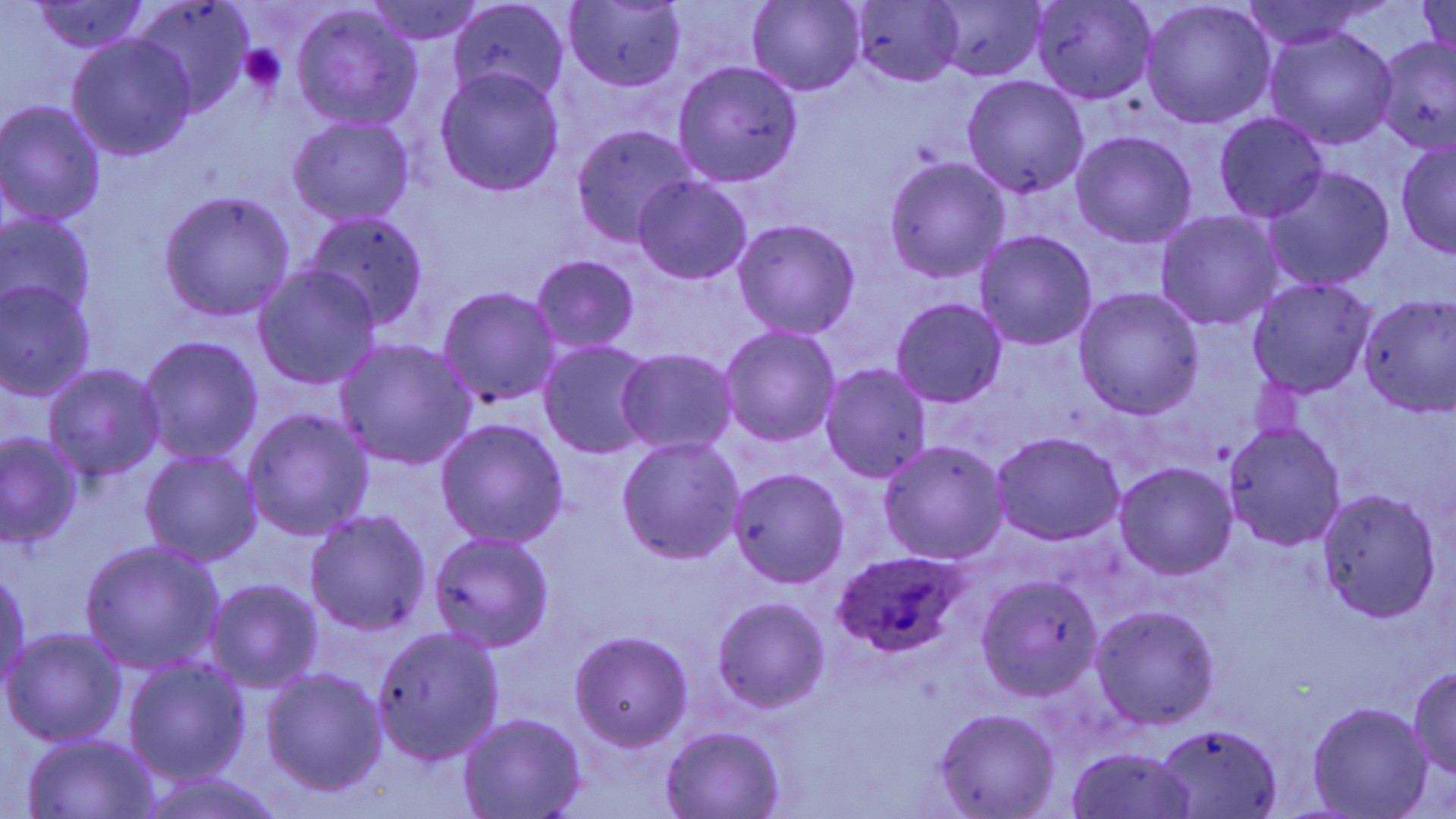
Approximate bounding boxes as (x1,y1)-(x2,y2) corner pairs in pixels. Uninfected red blood cell locations: (131,0)-(254,115), (365,0)-(489,45), (564,0)-(686,91), (746,0)-(865,96), (1031,0)-(1155,104), (1419,0)-(1454,62), (23,1)-(152,54), (449,2)-(571,106), (851,2)-(964,87), (927,2)-(1045,82), (1141,3)-(1276,127), (291,7)-(423,131), (1264,25)-(1400,148), (67,35)-(197,161), (1375,37)-(1455,155), (672,62)-(802,188), (435,68)-(565,196), (962,75)-(1090,198), (0,103)-(105,226), (1214,112)-(1330,222), (289,116)-(415,225), (571,125)-(696,245), (1070,130)-(1197,249), (1396,138)-(1455,257), (885,158)-(1010,283), (1263,164)-(1395,291), (635,177)-(752,284), (158,191)-(294,322), (307,210)-(429,326), (1155,211)-(1284,330), (1,213)-(98,321), (734,217)-(860,339), (977,230)-(1096,351), (532,255)-(639,354), (253,266)-(382,391), (1247,277)-(1379,396), (0,281)-(97,400), (437,285)-(562,408), (1073,288)-(1205,417), (1358,292)-(1456,416), (891,298)-(1007,408), (719,325)-(842,447), (139,337)-(263,463), (335,338)-(476,471), (538,341)-(659,459), (616,349)-(739,457), (44,363)-(166,481), (819,364)-(932,482), (242,408)-(373,542), (436,417)-(569,549), (1224,424)-(1345,552), (993,431)-(1125,544), (1,433)-(83,546), (616,437)-(745,565), (879,440)-(1009,564), (141,451)-(260,566), (1116,464)-(1236,578), (730,468)-(852,588), (1318,488)-(1441,623), (305,510)-(430,636), (429,533)-(555,652), (81,541)-(224,672), (1,562)-(31,697), (976,575)-(1104,700), (207,581)-(322,693), (713,598)-(829,713), (1090,607)-(1221,728), (370,627)-(505,767), (4,628)-(127,747), (570,632)-(692,750), (124,656)-(250,786), (261,668)-(388,796), (1408,669)-(1456,778), (1308,702)-(1433,817), (934,710)-(1058,818), (459,713)-(586,818), (1156,723)-(1283,817), (661,727)-(784,818), (21,734)-(162,816), (1065,746)-(1198,819). Platelet locations: (239,44)-(288,94). Plasmodium ovale-infected red blood cell locations: (831,550)-(969,657). Slide-level diagnosis: Plasmodium ovale. Image is 1456×819 pixels. Single field of view. May-Grünwald-Giemsa stain. Optical microscopy. 1000x magnification. Thin blood smear.